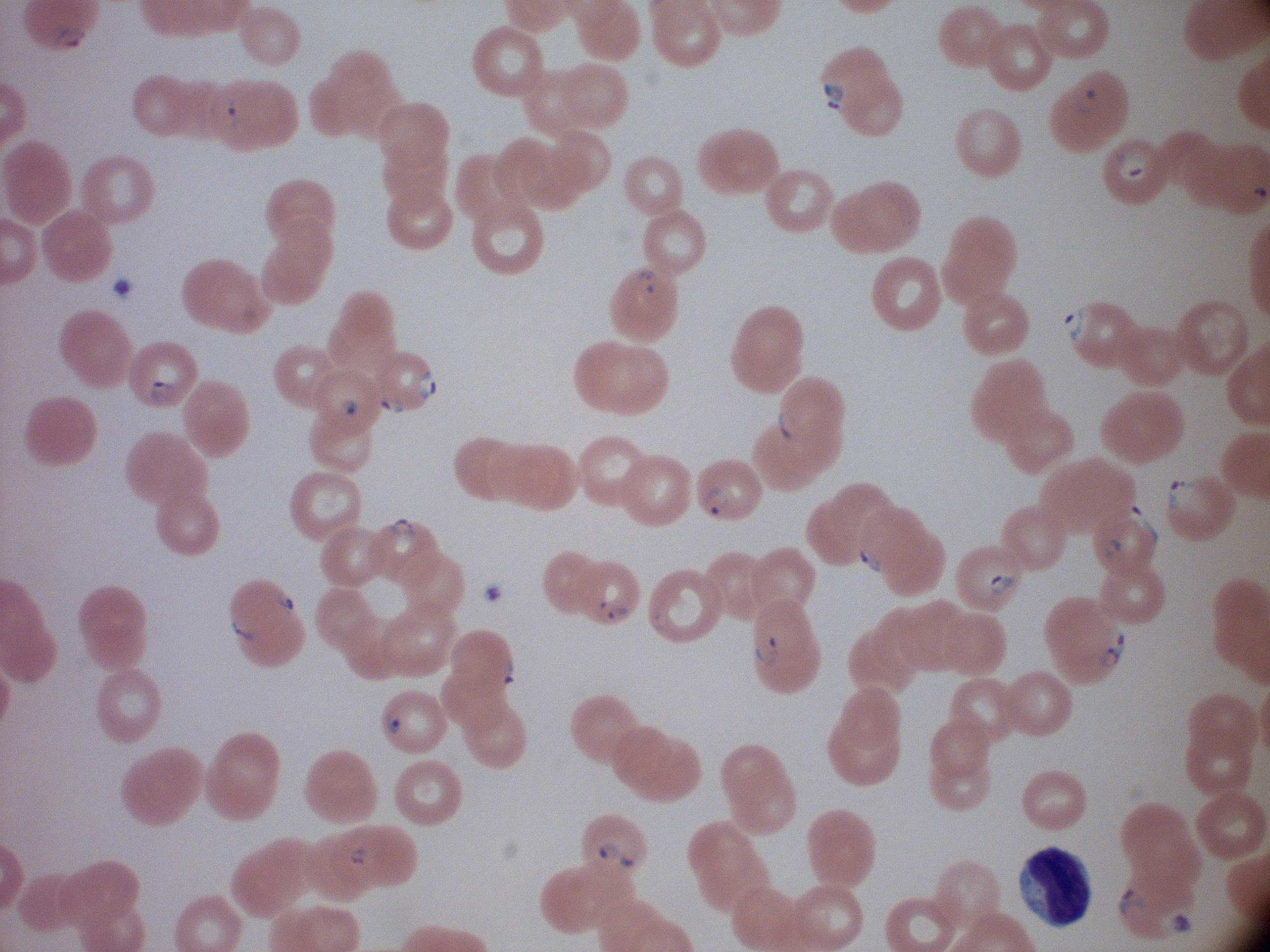 Approximate bounding boxes as named x1/y1/x2/y2 corners in pixels, from the source annotation, which is not necessarily exhaustive. Ring form locations: (x1=49, y1=23, x2=91, y2=52), (x1=818, y1=78, x2=851, y2=113), (x1=1072, y1=85, x2=1108, y2=123), (x1=205, y1=93, x2=241, y2=133), (x1=1112, y1=149, x2=1151, y2=185), (x1=630, y1=265, x2=663, y2=297), (x1=1058, y1=303, x2=1094, y2=349), (x1=409, y1=366, x2=445, y2=403), (x1=144, y1=374, x2=183, y2=407), (x1=373, y1=387, x2=412, y2=418), (x1=332, y1=391, x2=364, y2=426), (x1=775, y1=406, x2=800, y2=442), (x1=1161, y1=476, x2=1198, y2=512), (x1=696, y1=486, x2=738, y2=522), (x1=1122, y1=500, x2=1163, y2=551), (x1=381, y1=515, x2=422, y2=543), (x1=1100, y1=536, x2=1126, y2=563), (x1=854, y1=537, x2=884, y2=574), (x1=985, y1=571, x2=1018, y2=601), (x1=271, y1=586, x2=299, y2=621), (x1=594, y1=598, x2=631, y2=626), (x1=648, y1=604, x2=677, y2=636), (x1=225, y1=614, x2=259, y2=649), (x1=1100, y1=626, x2=1128, y2=670), (x1=750, y1=628, x2=785, y2=667), (x1=492, y1=653, x2=523, y2=690), (x1=380, y1=709, x2=409, y2=740), (x1=595, y1=839, x2=641, y2=871), (x1=345, y1=840, x2=375, y2=871), (x1=1115, y1=881, x2=1147, y2=923). Image is 1270×952 pixels. Acquired with a Leica DM2000 optical microscope and its built-in camera. Species: Plasmodium falciparum. Captured at 100x magnification. Thin blood film. One field from this slide. Giemsa stain.